Identify the preparation type.
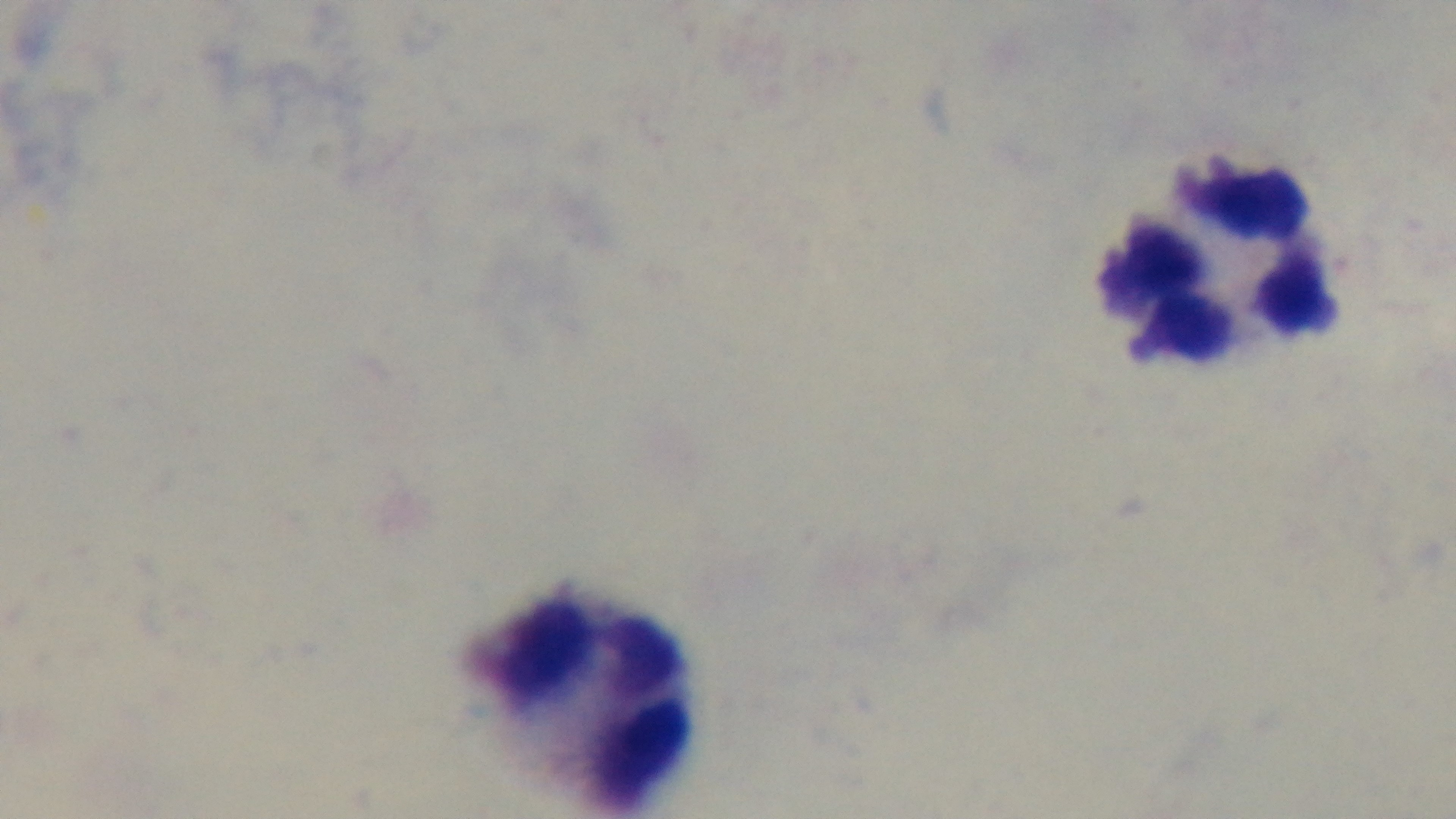
It is a thick blood film.

Light microscopy. Malaria status: negative. 100x oil-immersion objective. Captured with a mounted 4K digital camera. Giemsa stain. One field from the slide.